Assess this cell for malaria.
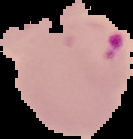
It is parasitized.

preparation = thin blood smear
image type = segmented cell region with the area outside set to black
image size = 133×139 pixels